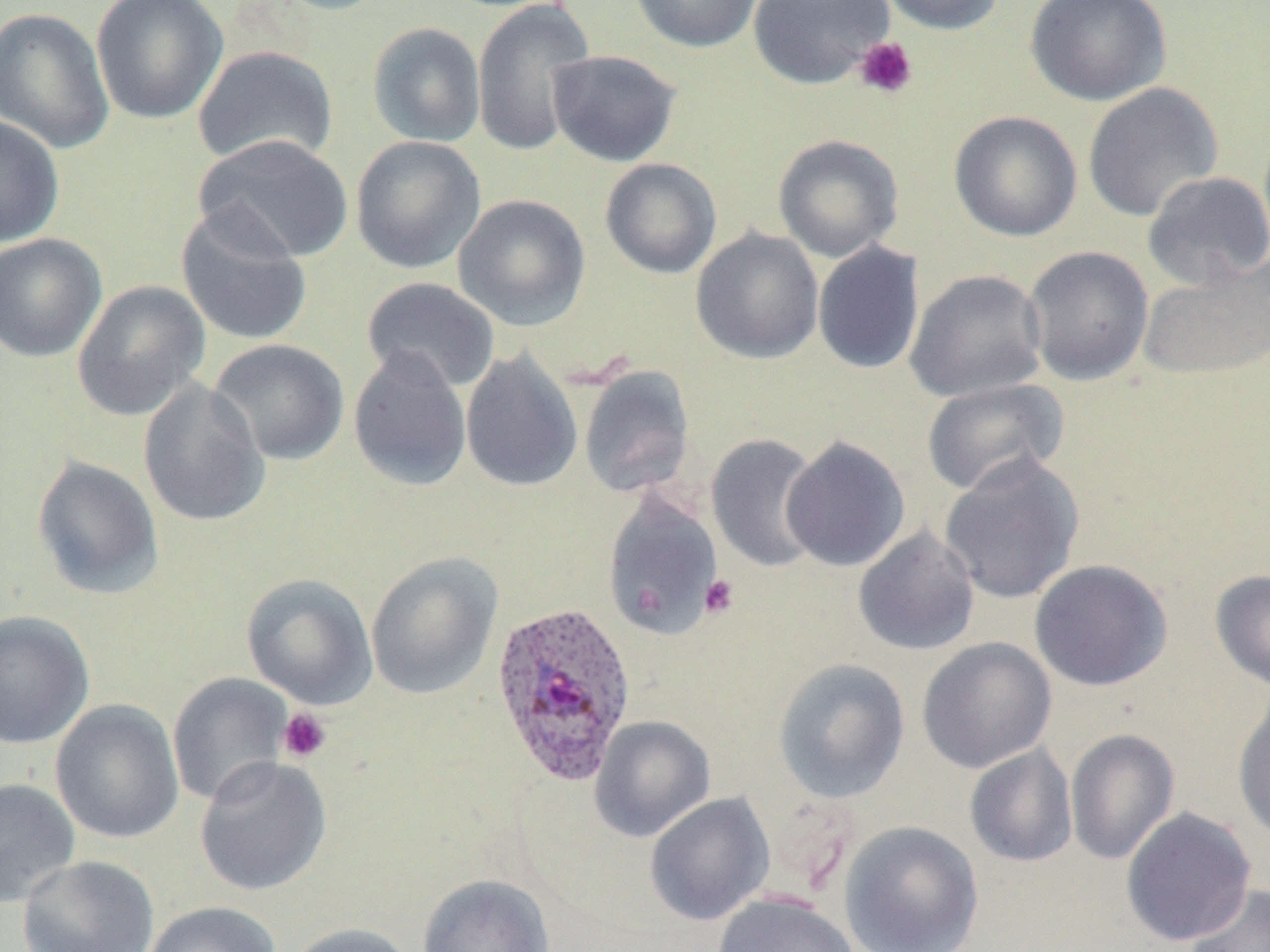 Approximate bounding boxes as named x1/y1/x2/y2 corners in pixels. Platelet locations: (x1=854, y1=36, x2=918, y2=99), (x1=699, y1=574, x2=740, y2=618), (x1=277, y1=707, x2=332, y2=763). Plasmodium ovale-infected red blood cell locations: (x1=491, y1=600, x2=637, y2=785). Uninfected red blood cell locations: (x1=90, y1=0, x2=228, y2=125), (x1=264, y1=0, x2=395, y2=16), (x1=471, y1=0, x2=596, y2=157), (x1=628, y1=0, x2=766, y2=53), (x1=748, y1=0, x2=894, y2=89), (x1=875, y1=0, x2=1008, y2=35), (x1=1026, y1=0, x2=1172, y2=107), (x1=0, y1=7, x2=115, y2=153), (x1=367, y1=21, x2=486, y2=148), (x1=192, y1=45, x2=339, y2=167), (x1=546, y1=49, x2=682, y2=167), (x1=1082, y1=82, x2=1224, y2=222), (x1=948, y1=110, x2=1083, y2=242), (x1=0, y1=114, x2=64, y2=248), (x1=192, y1=134, x2=354, y2=264), (x1=773, y1=134, x2=904, y2=262), (x1=350, y1=135, x2=486, y2=273), (x1=599, y1=158, x2=722, y2=279), (x1=1141, y1=171, x2=1270, y2=290), (x1=453, y1=193, x2=591, y2=331), (x1=176, y1=205, x2=313, y2=346), (x1=691, y1=228, x2=824, y2=364), (x1=0, y1=233, x2=107, y2=363), (x1=813, y1=242, x2=925, y2=374), (x1=1022, y1=245, x2=1154, y2=386), (x1=1138, y1=259, x2=1270, y2=382), (x1=905, y1=269, x2=1048, y2=403), (x1=360, y1=277, x2=500, y2=395), (x1=72, y1=280, x2=211, y2=421), (x1=208, y1=338, x2=350, y2=466), (x1=347, y1=348, x2=472, y2=491), (x1=460, y1=350, x2=583, y2=492), (x1=578, y1=365, x2=696, y2=499), (x1=921, y1=378, x2=1069, y2=498), (x1=137, y1=379, x2=271, y2=528), (x1=705, y1=433, x2=826, y2=572), (x1=780, y1=436, x2=911, y2=572), (x1=939, y1=454, x2=1084, y2=604), (x1=31, y1=456, x2=165, y2=601), (x1=601, y1=490, x2=724, y2=640), (x1=852, y1=525, x2=981, y2=656), (x1=366, y1=552, x2=502, y2=700), (x1=1029, y1=559, x2=1173, y2=692), (x1=1210, y1=569, x2=1270, y2=691), (x1=241, y1=572, x2=378, y2=709), (x1=0, y1=610, x2=95, y2=749), (x1=917, y1=637, x2=1057, y2=774), (x1=772, y1=658, x2=911, y2=803), (x1=167, y1=673, x2=294, y2=808), (x1=1232, y1=692, x2=1270, y2=845), (x1=50, y1=699, x2=184, y2=845), (x1=589, y1=716, x2=716, y2=841), (x1=1065, y1=727, x2=1180, y2=865), (x1=964, y1=744, x2=1078, y2=868), (x1=194, y1=755, x2=332, y2=896), (x1=0, y1=777, x2=81, y2=908), (x1=644, y1=792, x2=775, y2=926), (x1=1120, y1=806, x2=1257, y2=947), (x1=840, y1=820, x2=984, y2=952), (x1=18, y1=855, x2=160, y2=951), (x1=416, y1=873, x2=555, y2=952), (x1=1184, y1=883, x2=1270, y2=952), (x1=712, y1=892, x2=861, y2=952), (x1=142, y1=901, x2=281, y2=952), (x1=284, y1=922, x2=416, y2=952). Slide-level diagnosis: Plasmodium ovale. Thin blood smear. May-Grünwald-Giemsa stain. 1000x magnification. Image is 1270×952 pixels. One field of a larger specimen. Light microscopy.